Identify the cell.
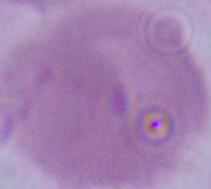
An erythrocyte.

modality: micrograph
magnification: 1000x